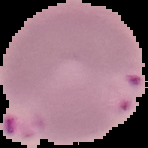

Cell region segmented out of the field of view; the surrounding area is masked to black. Result: malaria parasites identified. From a thin blood film. Image is 148×148 pixels.